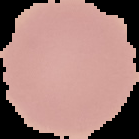
Summary:
  - Image type: segmented cell region on a black background
  - Result: negative for malaria parasites
  - Preparation: thin blood smear
  - Image size: 139×139 pixels